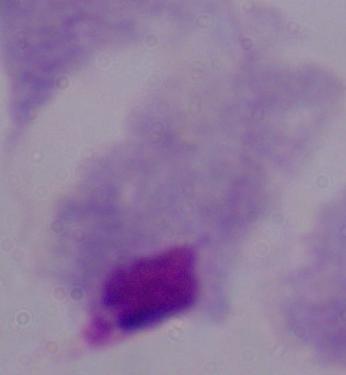

magnification = 1000x
identification = trichomonad
modality = photomicrograph